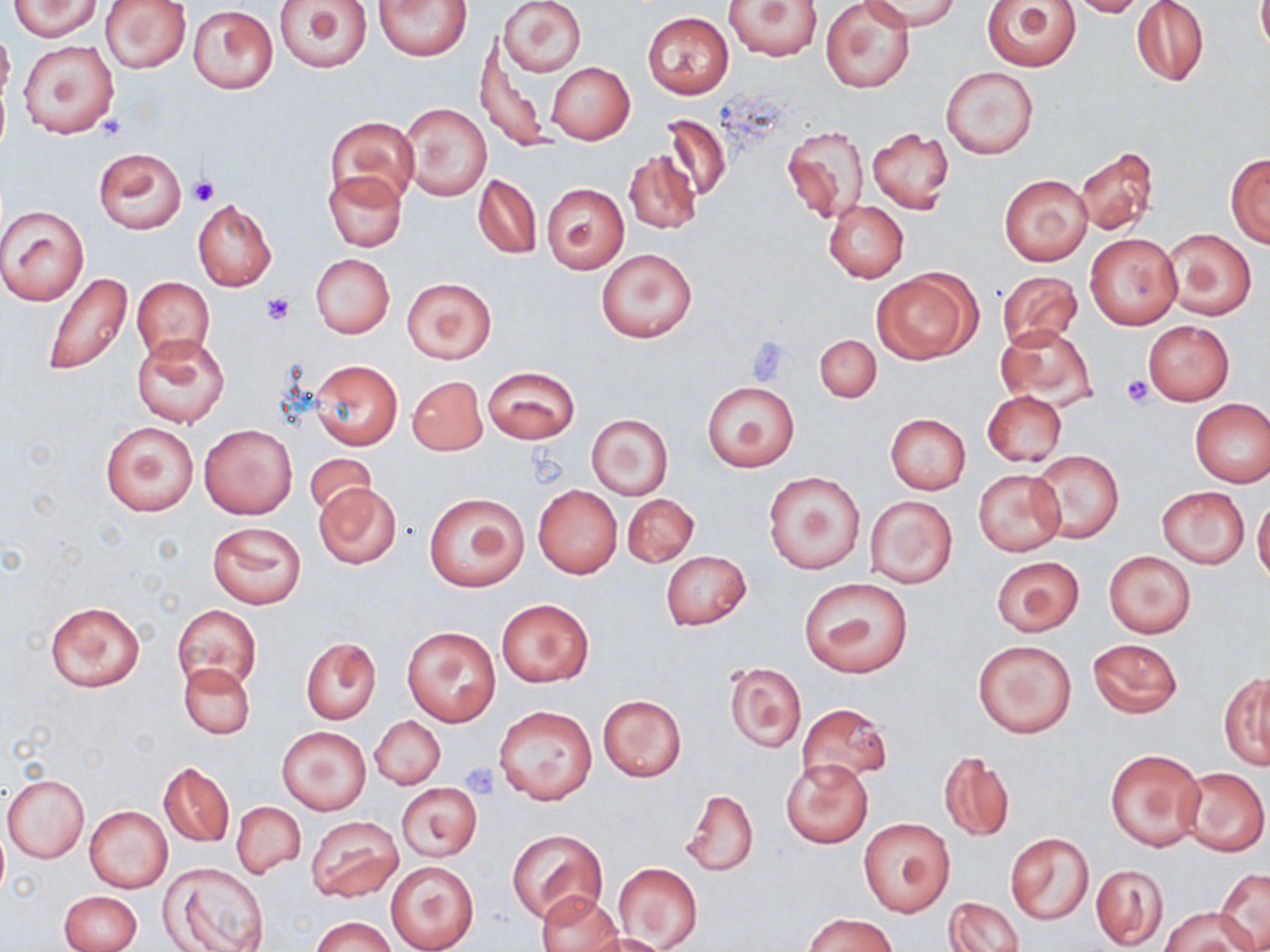 Approximate bounding boxes as [x1, y1, x2, y2] in pixels. Uninfected red blood cell locations: [8, 0, 101, 39], [101, 0, 192, 74], [275, 0, 373, 72], [373, 0, 473, 61], [498, 0, 586, 77], [821, 0, 915, 92], [862, 0, 959, 31], [983, 0, 1082, 70], [1064, 0, 1149, 17], [725, 1, 822, 61], [1131, 1, 1210, 87], [1257, 1, 1270, 57], [188, 4, 278, 94], [641, 11, 734, 98], [0, 26, 14, 104], [18, 39, 118, 138], [478, 42, 549, 154], [546, 62, 635, 144], [940, 67, 1040, 160], [400, 102, 492, 201], [658, 113, 732, 203], [326, 116, 419, 209], [782, 124, 869, 224], [867, 128, 955, 214], [1076, 147, 1159, 235], [94, 148, 186, 232], [624, 150, 701, 235], [1226, 153, 1270, 246], [324, 170, 406, 251], [474, 174, 541, 259], [999, 174, 1092, 265], [541, 182, 630, 273], [192, 200, 276, 292], [823, 201, 908, 283], [0, 205, 90, 304], [1163, 228, 1256, 320], [1084, 232, 1183, 330], [597, 246, 696, 343], [310, 254, 394, 339], [873, 268, 981, 363], [39, 270, 137, 377], [996, 271, 1082, 349], [132, 276, 214, 361], [402, 277, 497, 365], [1144, 320, 1234, 405], [997, 326, 1098, 411], [131, 335, 230, 427], [814, 335, 881, 402], [309, 359, 402, 450], [482, 365, 579, 444], [408, 375, 487, 455], [702, 382, 799, 471], [981, 390, 1066, 467], [1190, 399, 1270, 487], [885, 413, 971, 494], [587, 414, 673, 498], [99, 421, 199, 516], [198, 423, 298, 520], [1028, 449, 1123, 544], [304, 454, 380, 520], [973, 469, 1065, 556], [764, 472, 864, 573], [312, 481, 404, 570], [533, 485, 621, 578], [1157, 486, 1249, 568], [424, 493, 528, 591], [623, 494, 698, 567], [865, 495, 958, 588], [1253, 499, 1270, 586], [208, 521, 307, 609], [660, 550, 752, 631], [1102, 550, 1196, 638], [991, 556, 1084, 636], [798, 577, 913, 678], [495, 598, 594, 687], [45, 601, 146, 692], [172, 605, 262, 692], [401, 625, 501, 727], [972, 638, 1076, 738], [1087, 638, 1183, 719], [301, 639, 381, 725], [724, 661, 806, 752], [180, 662, 255, 738], [1219, 672, 1270, 769], [597, 694, 687, 781], [798, 703, 892, 785], [494, 705, 597, 805], [371, 715, 445, 790], [276, 724, 372, 815], [1105, 747, 1205, 851], [938, 751, 1015, 843], [781, 759, 872, 848], [160, 762, 233, 847], [1180, 767, 1268, 856], [2, 775, 88, 863], [396, 783, 483, 861], [679, 789, 758, 876], [231, 801, 305, 879], [85, 806, 173, 893], [307, 816, 402, 903], [859, 818, 954, 917], [508, 829, 607, 924], [1005, 832, 1094, 924], [386, 860, 478, 952], [160, 863, 271, 952], [613, 863, 703, 951], [1090, 863, 1168, 949], [1216, 867, 1269, 950], [58, 890, 141, 952], [536, 892, 623, 952], [943, 896, 1025, 952], [1160, 907, 1255, 952], [802, 913, 900, 952], [311, 916, 394, 952], [583, 931, 670, 952]. Platelet locations: [189, 176, 218, 207], [262, 292, 296, 325], [745, 338, 793, 384], [1122, 375, 1156, 405], [461, 764, 500, 797]. Slide-level diagnosis: negative for blood parasites. Light microscopy. Image is 1270×952 pixels. 1000x magnification. May-Grünwald-Giemsa-stained preparation. Thin blood smear. One field of a larger specimen.